Report the malaria status of this cell.
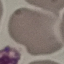

Uninfected.

Summary:
  - Image type: cell patch, automatically extracted from a larger field of view and resized to 64 × 64 pixels
  - Capture: smartphone camera at the microscope eyepiece
  - Preparation: thin blood smear
  - Stain: Giemsa